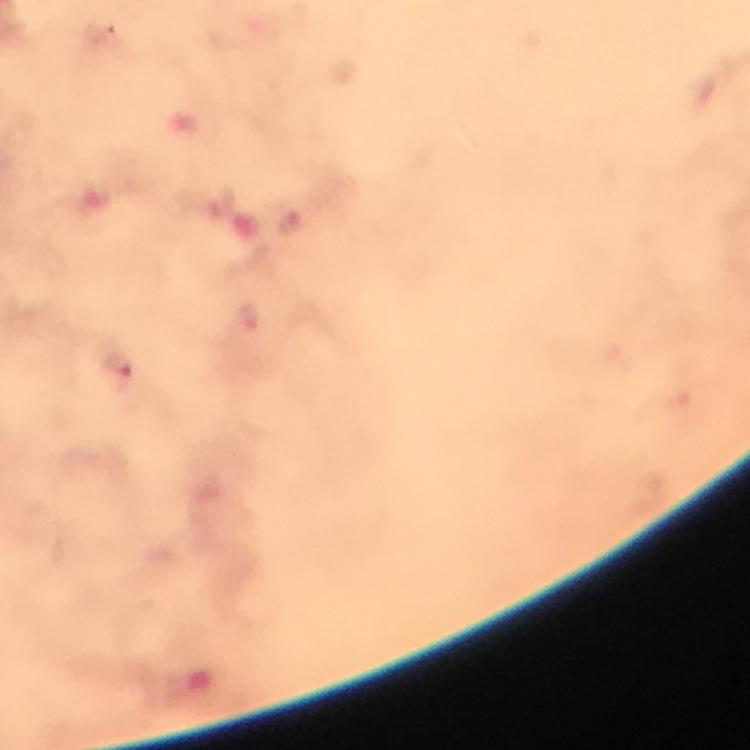

Approximate centers as [x, y] in pixels.
Summary:
  - Malaria parasite locations: [250, 318], [119, 365]
  - Cropped from: a single field of view
  - Context: from a malaria diagnostic workup
  - Image size: 750×750 pixels
  - Immersion oil: applied
  - Preparation: thick blood film
  - Stain: Giemsa
  - Capture: smartphone mounted on the microscope
  - Magnification: 100x